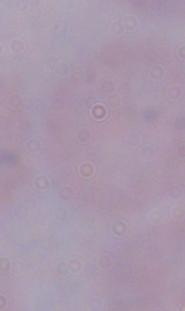
identification = trypanosome
magnification = 1000x
modality = photomicrograph